Locate every Plasmodium vivax-infected red blood cell.
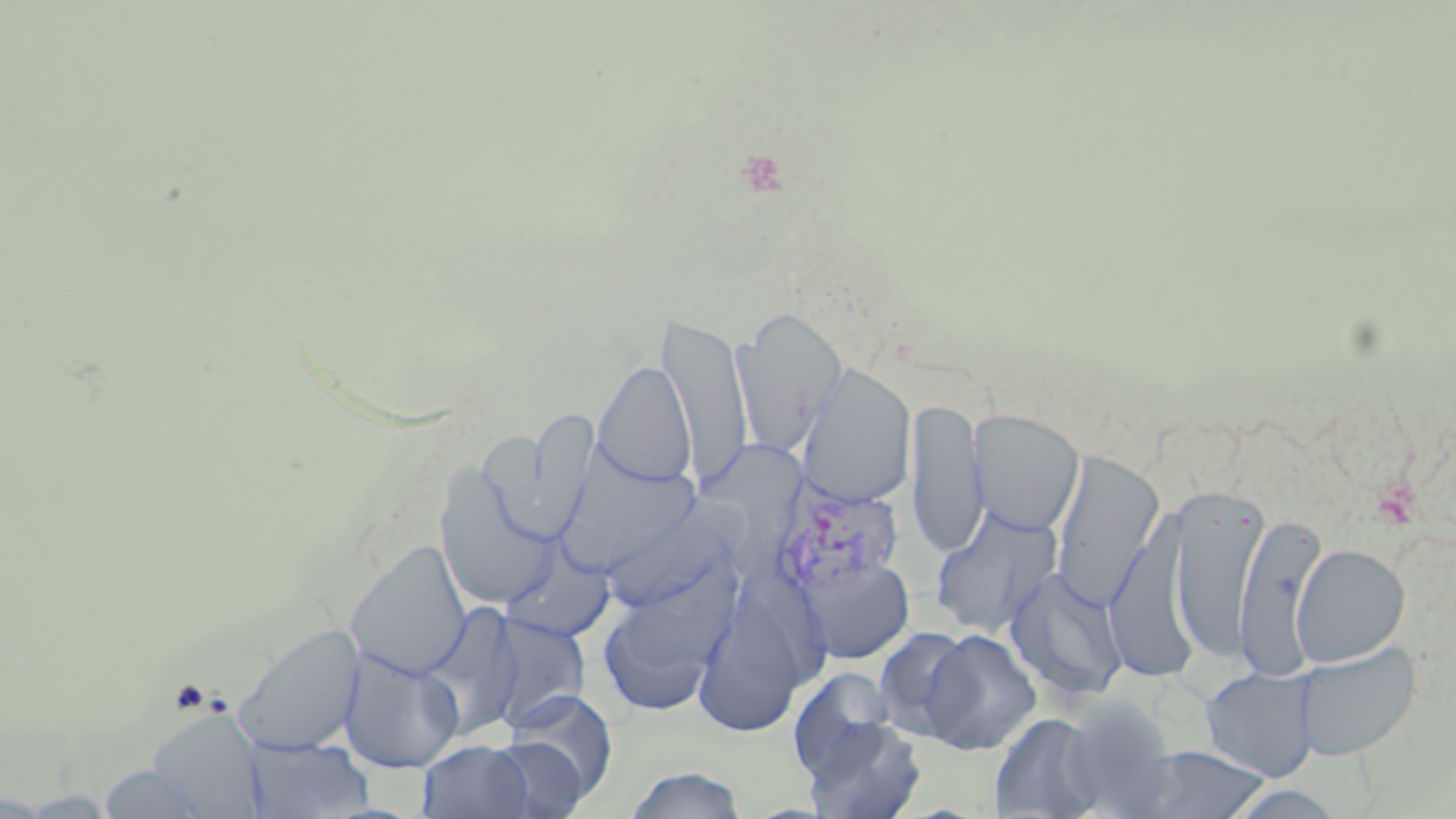

Approximate bounding boxes as named x1/y1/x2/y2 corners in pixels.
Plasmodium vivax-infected red blood cells: (x1=774, y1=476, x2=905, y2=600).

Summary:
  - Uninfected red blood cell locations: (x1=733, y1=306, x2=847, y2=456), (x1=660, y1=313, x2=753, y2=490), (x1=593, y1=360, x2=696, y2=488), (x1=797, y1=363, x2=916, y2=507), (x1=906, y1=396, x2=988, y2=557), (x1=516, y1=407, x2=599, y2=545), (x1=968, y1=409, x2=1085, y2=536), (x1=1050, y1=450, x2=1165, y2=610), (x1=552, y1=452, x2=706, y2=578), (x1=434, y1=463, x2=560, y2=611), (x1=1168, y1=481, x2=1268, y2=667), (x1=610, y1=493, x2=759, y2=613), (x1=1105, y1=502, x2=1202, y2=684), (x1=930, y1=503, x2=1063, y2=638), (x1=1235, y1=511, x2=1329, y2=680), (x1=345, y1=540, x2=472, y2=682), (x1=499, y1=540, x2=616, y2=644), (x1=1291, y1=543, x2=1411, y2=667), (x1=796, y1=553, x2=915, y2=664), (x1=596, y1=556, x2=738, y2=717), (x1=1005, y1=566, x2=1129, y2=704), (x1=694, y1=601, x2=812, y2=736), (x1=417, y1=603, x2=524, y2=739), (x1=485, y1=613, x2=591, y2=729), (x1=231, y1=622, x2=366, y2=757), (x1=872, y1=626, x2=978, y2=743), (x1=920, y1=629, x2=1041, y2=755), (x1=1291, y1=641, x2=1421, y2=761), (x1=338, y1=645, x2=465, y2=774), (x1=1201, y1=666, x2=1320, y2=781), (x1=787, y1=667, x2=897, y2=783), (x1=501, y1=689, x2=618, y2=805), (x1=1059, y1=696, x2=1180, y2=816), (x1=149, y1=712, x2=266, y2=816), (x1=990, y1=712, x2=1108, y2=818), (x1=801, y1=714, x2=927, y2=818), (x1=243, y1=736, x2=373, y2=818), (x1=484, y1=736, x2=589, y2=819), (x1=418, y1=739, x2=535, y2=819), (x1=1128, y1=744, x2=1271, y2=819), (x1=97, y1=761, x2=215, y2=819), (x1=624, y1=765, x2=748, y2=819), (x1=1221, y1=784, x2=1347, y2=818)
  - Slide-level diagnosis: Plasmodium vivax
  - Preparation: thin blood smear
  - Modality: optical microscopy
  - Field of view: one of a larger specimen
  - Image size: 1456×819 pixels
  - Magnification: 1000x
  - Stain: May-Grünwald-Giemsa